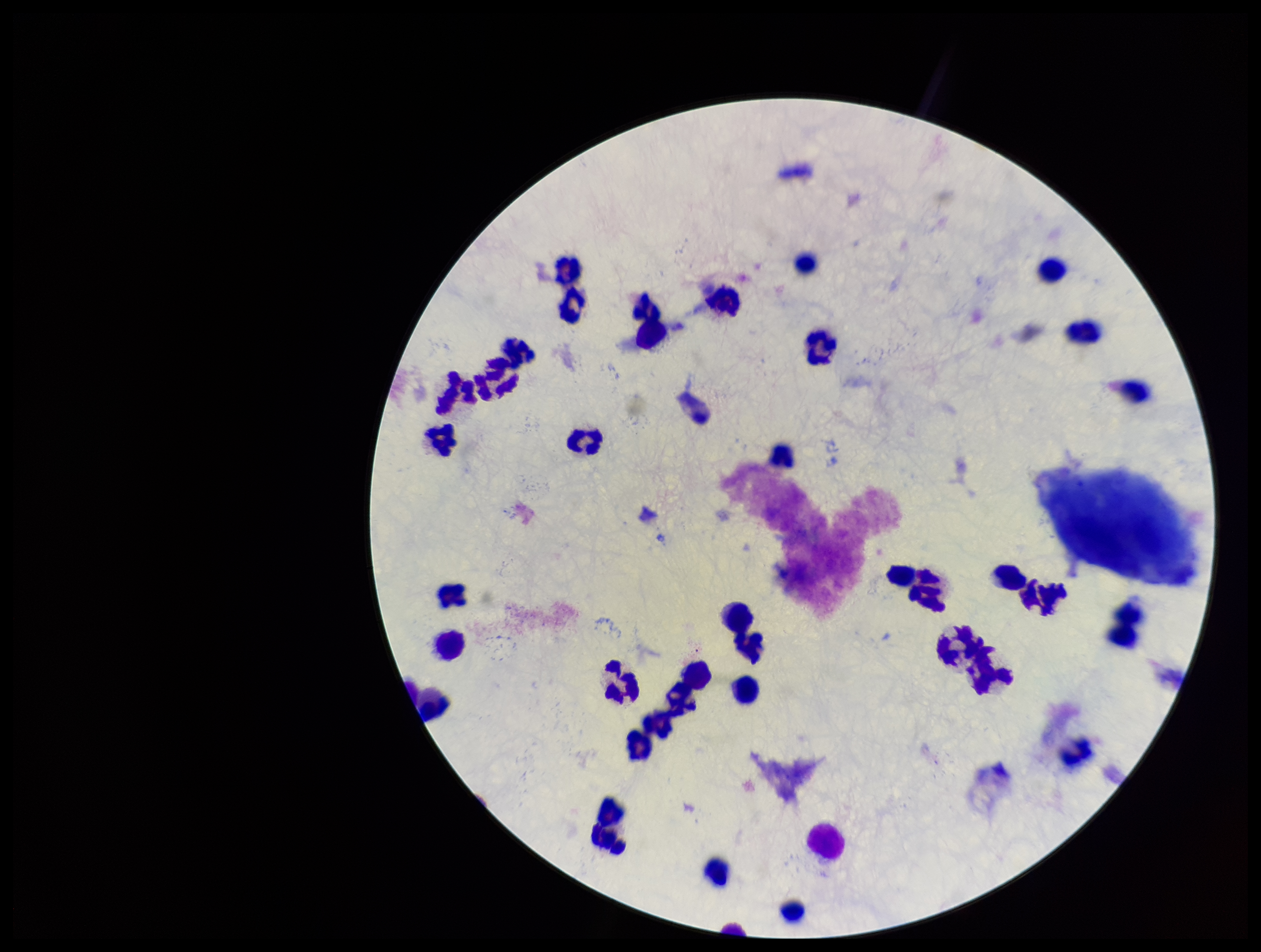
Summary:
  - Parasite count: 0
  - Field of view: single
  - Stain: Giemsa
  - Image size: 1261×952 pixels
  - Plasmodium parasites: none detected
  - Patient malaria status: negative
  - Capture: smartphone photograph through the microscope eyepiece
  - Leukocyte count: 33
  - Preparation: thick blood smear